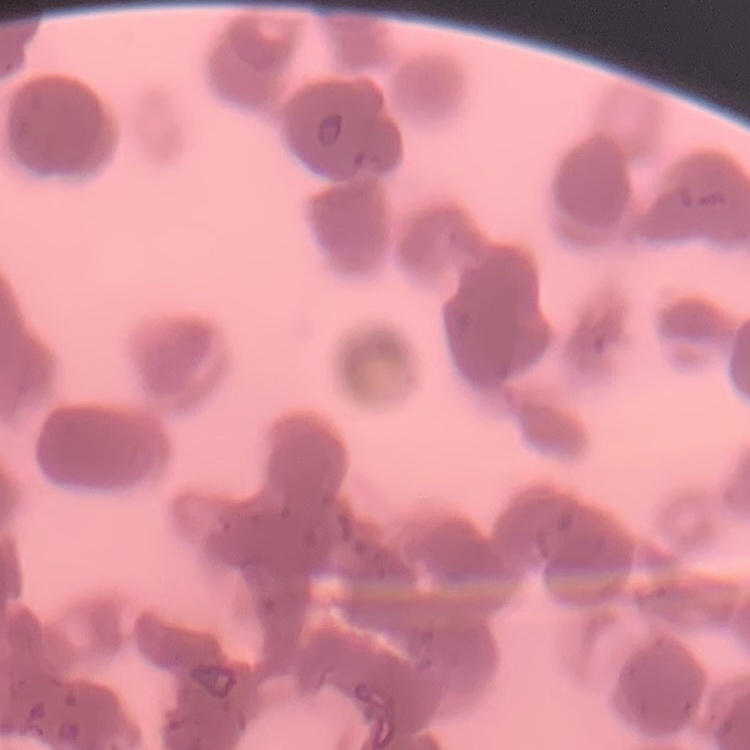

red blood cell morphology = rouleaux formation
stain = Field's or Giemsa
image type = square crop of a larger photomicrograph
preparation = thin blood smear